Identify the parasite.
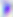
Toxoplasma gondii.

{
  "magnification": "400x",
  "modality": "photomicrograph"
}